Locate every Plasmodium parasite.
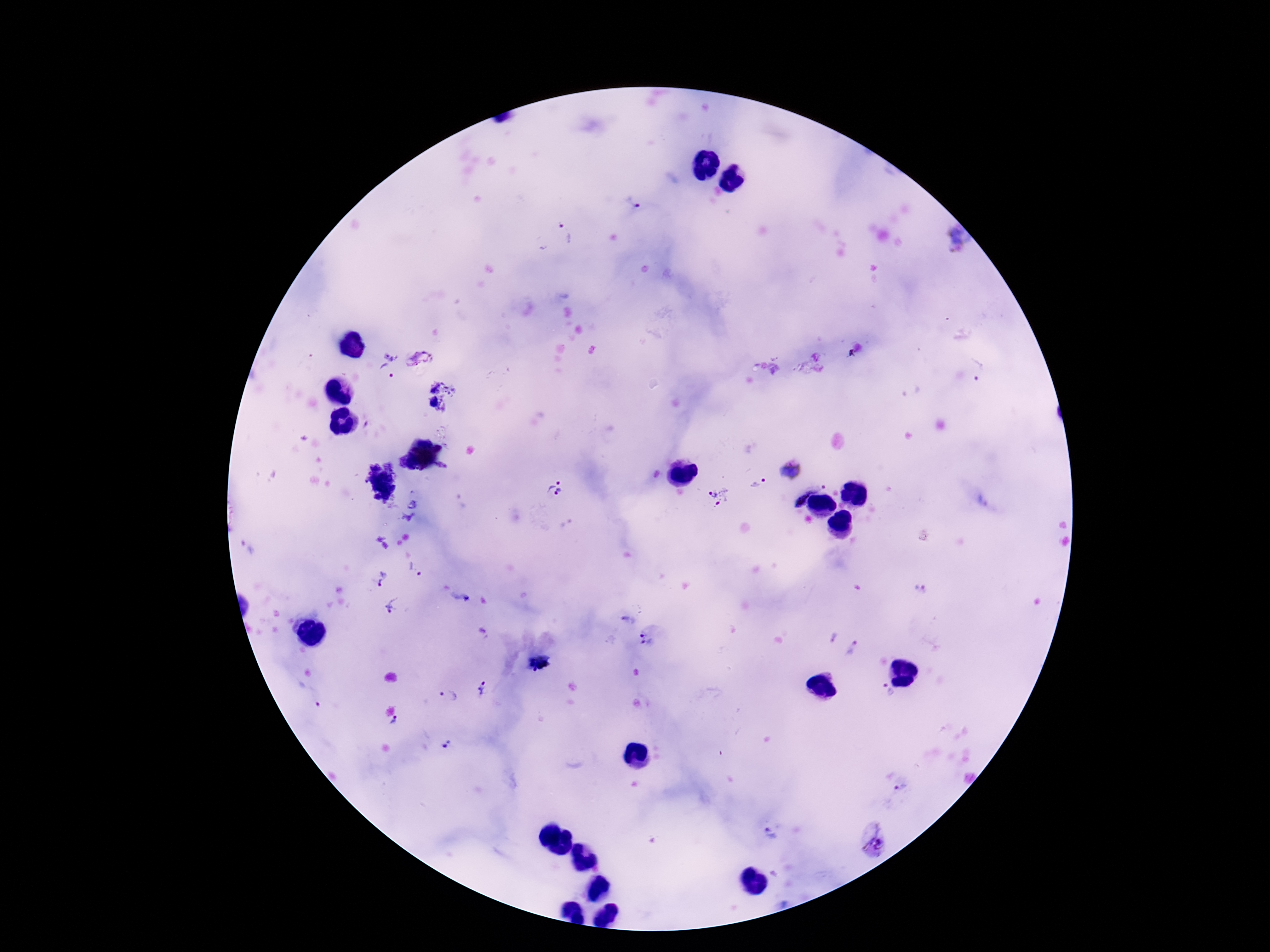

Approximate centers as {x, y} in pixels.
Plasmodium parasites: {632, 203}, {566, 233}, {392, 352}, {419, 359}, {387, 373}, {434, 390}, {432, 403}, {790, 470}, {757, 484}, {555, 489}, {718, 497}, {809, 497}, {415, 571}, {383, 578}, {920, 588}, {393, 607}, {832, 637}, {651, 640}, {854, 650}, {483, 688}, {306, 694}, {884, 694}, {449, 696}, {393, 723}, {447, 743}, {901, 788}, {771, 834}, {874, 844}.

Thick peripheral-blood smear. Image is 1270×952 pixels. 100x magnification. Giemsa-stained preparation. Single field of view. Patient malaria status: positive. Photographed through the microscope eyepiece with a smartphone camera.